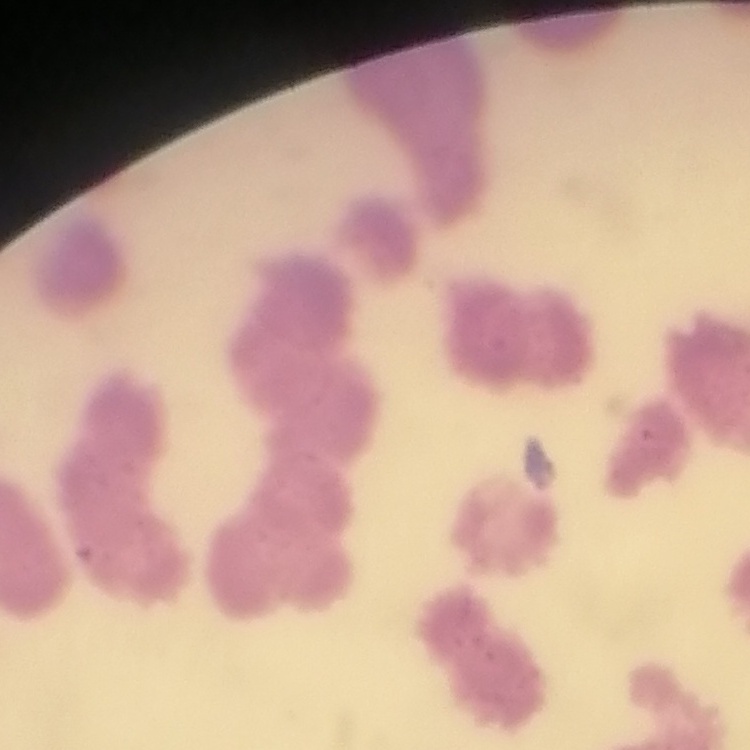
The red blood cells exhibit rouleaux formation. Thin peripheral smear. Field's or Giemsa stain. Square crop of a larger photomicrograph.